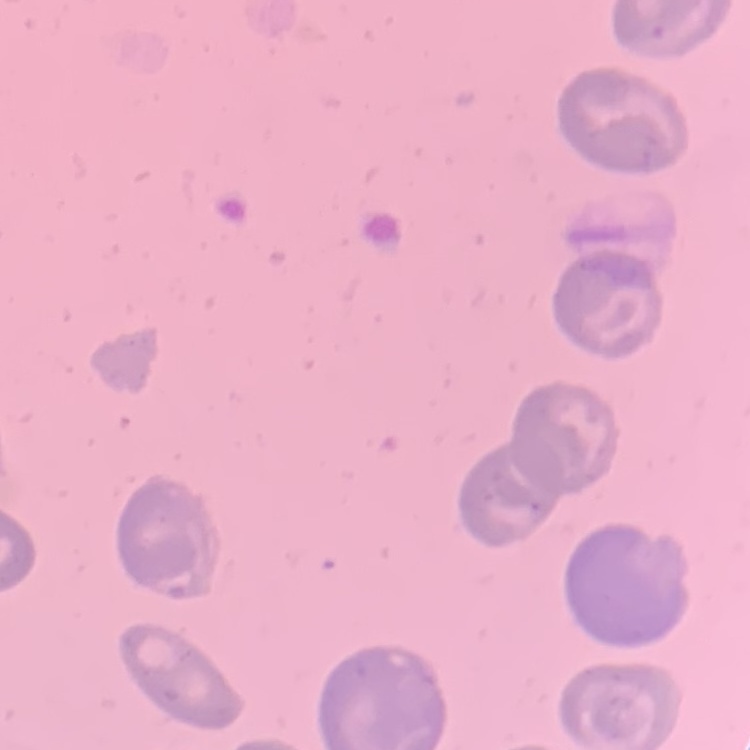

The red blood cells show no rouleaux formation. Thin blood smear. Field's or Giemsa stain. One tile cut from a larger photomicrograph.